State the blood parasite species.
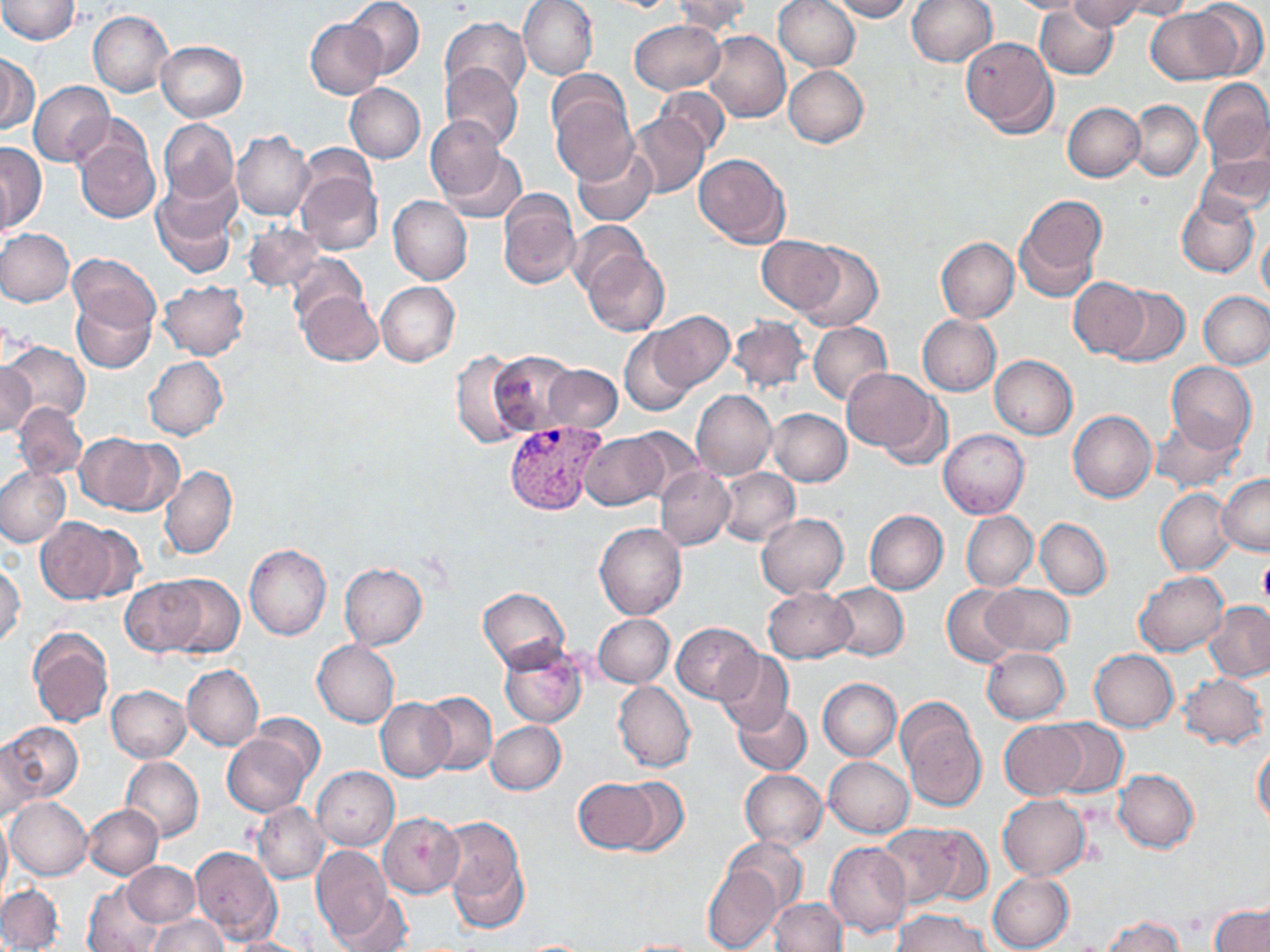
Plasmodium vivax.

stain: May-Grünwald-Giemsa
magnification: 1000x
uninfected_red_blood_cell_locations: 'approximate bounding boxes as (x1,y1)-(x2,y2) corner pairs in pixels: (0,0)-(80,44), (343,0)-(425,79), (518,0)-(598,80), (672,0)-(750,37), (772,0)-(860,72), (828,0)-(912,20), (906,0)-(998,67), (1001,0)-(1096,14), (1068,0)-(1147,31), (1116,0)-(1199,20), (1194,2)-(1267,76), (1034,5)-(1118,79), (1146,7)-(1242,84), (89,11)-(173,96), (446,11)-(598,88), (440,17)-(531,102), (306,19)-(386,99), (629,19)-(724,95), (704,30)-(791,123), (960,36)-(1058,138), (156,41)-(247,122), (0,55)-(37,134), (441,62)-(524,150), (784,65)-(869,147), (547,69)-(628,141), (1199,77)-(1270,167), (28,80)-(113,167), (344,83)-(425,163), (654,85)-(731,155), (549,91)-(637,185), (1129,99)-(1204,181), (1063,102)-(1145,181), (629,115)-(710,198), (424,117)-(508,201), (158,118)-(239,205), (70,126)-(161,225), (233,131)-(314,221), (0,140)-(46,232), (296,142)-(377,214), (573,146)-(658,227), (441,149)-(528,225), (1198,152)-(1270,223), (693,153)-(789,249), (295,167)-(382,255), (151,177)-(239,278), (497,189)-(580,289), (388,195)-(472,284), (1176,195)-(1259,278), (1014,197)-(1104,300), (568,220)-(647,297), (243,222)-(325,292), (0,228)-(74,305), (1257,228)-(1270,304), (756,236)-(843,315), (936,237)-(1019,322), (796,241)-(882,331), (581,249)-(670,336), (69,252)-(159,333), (286,252)-(366,326), (1068,276)-(1149,359), (158,280)-(250,360), (376,281)-(459,366), (1107,285)-(1191,367), (298,290)-(383,366), (1200,291)-(1270,368), (72,292)-(155,372), (648,311)-(734,391), (728,314)-(811,394), (917,314)-(1001,396), (809,321)-(893,404), (619,328)-(701,416), (4,340)-(90,425), (452,351)-(533,449), (488,351)-(580,436), (990,355)-(1077,439), (144,356)-(228,440), (0,360)-(36,438), (1166,362)-(1256,453), (543,365)-(622,433), (842,368)-(941,457), (692,390)-(777,480), (13,402)-(88,480), (768,408)-(851,486), (1069,410)-(1157,502), (1151,416)-(1245,493), (625,428)-(705,503), (938,429)-(1030,517), (74,433)-(167,514), (579,433)-(667,511), (160,464)-(238,561), (0,466)-(70,549), (655,466)-(734,551), (718,467)-(799,546), (1217,473)-(1270,556), (1155,487)-(1236,575), (865,510)-(948,595), (961,511)-(1038,591), (756,513)-(848,597), (35,517)-(129,604), (1035,518)-(1112,600), (594,522)-(687,621), (244,544)-(332,640), (339,562)-(428,650), (0,564)-(26,647), (1134,570)-(1227,657), (161,575)-(244,658), (121,578)-(204,656), (828,583)-(908,660), (981,583)-(1074,656), (942,584)-(1022,668), (762,586)-(856,663), (479,588)-(570,673), (1205,600)-(1270,683), (593,613)-(673,687), (673,622)-(763,704), (27,627)-(112,728), (312,639)-(399,728), (499,643)-(587,728), (982,647)-(1070,724), (1088,649)-(1179,732), (713,650)-(795,736), (182,664)-(264,751), (1178,673)-(1267,750), (819,678)-(901,760), (613,681)-(695,773), (106,685)-(192,763), (417,691)-(497,775), (376,698)-(454,781), (732,700)-(812,775), (898,704)-(986,815), (487,720)-(566,794), (999,720)-(1086,798), (1046,720)-(1127,796), (3,723)-(82,803), (221,729)-(314,815), (0,737)-(38,825), (1253,743)-(1270,830), (121,755)-(203,842), (824,757)-(914,838), (311,766)-(399,850), (738,769)-(827,851), (1113,769)-(1198,853), (574,777)-(662,853), (613,778)-(688,855), (997,794)-(1090,879), (5,797)-(92,880), (252,803)-(329,883), (83,804)-(163,880), (378,812)-(464,898), (0,814)-(10,902), (440,814)-(532,931), (878,822)-(969,909), (917,825)-(992,907), (723,836)-(808,917), (825,842)-(911,937), (311,846)-(392,940), (189,847)-(282,946), (123,861)-(200,926), (703,866)-(781,951), (987,871)-(1075,952), (81,881)-(165,952), (0,883)-(63,951), (330,889)-(417,952), (769,898)-(847,951), (1210,903)-(1270,952), (893,910)-(992,952), (147,914)-(228,952), (1099,915)-(1185,952), (227,935)-(315,952), (620,937)-(706,951), (514,939)-(601,951)'
modality: light microscopy
plasmodium_vivax_infected_red_blood_cell_locations: 'approximate bounding boxes as (x1,y1)-(x2,y2) corner pairs in pixels: (502,419)-(605,516)'
field_of_view: one of a larger specimen
image_size: 1270×952 pixels
preparation: thin blood film
platelet_locations: 'approximate bounding boxes as (x1,y1)-(x2,y2) corner pairs in pixels: (1257,558)-(1270,605)'